Outline each Plasmodium falciparum-infected red blood cell.
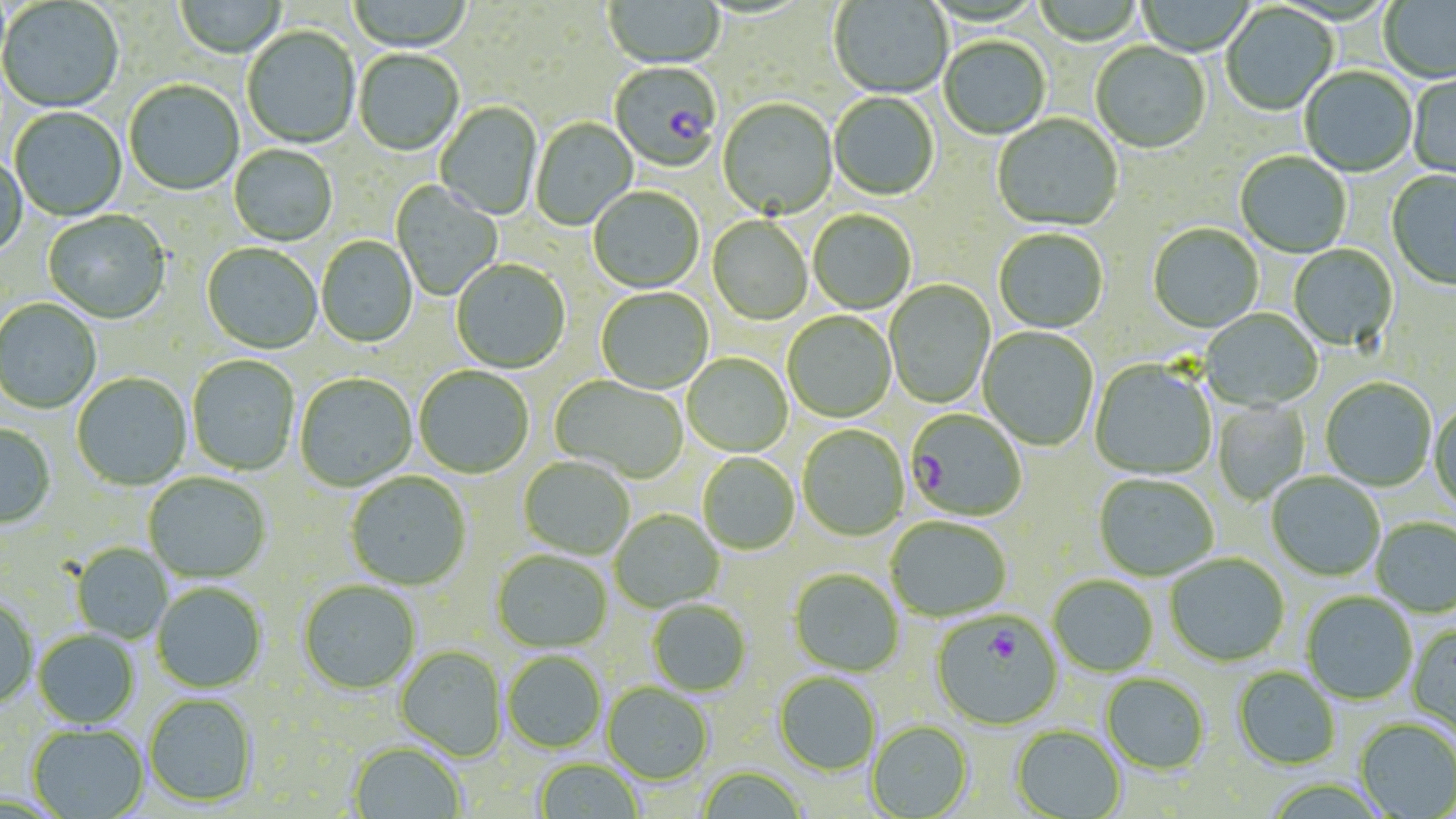

Approximate bounding boxes as named x1/y1/x2/y2 corners in pixels.
Plasmodium falciparum-infected red blood cells: (x1=609, y1=63, x2=721, y2=174), (x1=905, y1=410, x2=1026, y2=522), (x1=932, y1=612, x2=1061, y2=730).

Summary:
  - Uninfected red blood cell locations: (x1=174, y1=0, x2=286, y2=59), (x1=347, y1=0, x2=473, y2=53), (x1=1030, y1=0, x2=1145, y2=47), (x1=1135, y1=0, x2=1257, y2=56), (x1=1379, y1=0, x2=1456, y2=85), (x1=0, y1=1, x2=124, y2=115), (x1=604, y1=1, x2=726, y2=71), (x1=829, y1=1, x2=952, y2=100), (x1=1220, y1=4, x2=1338, y2=117), (x1=242, y1=27, x2=360, y2=150), (x1=939, y1=38, x2=1051, y2=141), (x1=1091, y1=42, x2=1211, y2=156), (x1=354, y1=50, x2=464, y2=157), (x1=1299, y1=68, x2=1417, y2=178), (x1=1408, y1=73, x2=1456, y2=182), (x1=124, y1=81, x2=244, y2=197), (x1=829, y1=93, x2=939, y2=201), (x1=717, y1=99, x2=838, y2=222), (x1=435, y1=102, x2=543, y2=221), (x1=10, y1=108, x2=127, y2=221), (x1=992, y1=115, x2=1123, y2=233), (x1=530, y1=117, x2=638, y2=231), (x1=228, y1=145, x2=337, y2=247), (x1=1235, y1=152, x2=1351, y2=258), (x1=0, y1=156, x2=27, y2=260), (x1=1387, y1=170, x2=1456, y2=292), (x1=391, y1=181, x2=502, y2=301), (x1=589, y1=188, x2=704, y2=294), (x1=42, y1=211, x2=171, y2=324), (x1=808, y1=211, x2=916, y2=315), (x1=707, y1=217, x2=813, y2=326), (x1=1148, y1=225, x2=1263, y2=334), (x1=994, y1=230, x2=1108, y2=335), (x1=316, y1=237, x2=418, y2=348), (x1=201, y1=244, x2=322, y2=355), (x1=1289, y1=245, x2=1398, y2=352), (x1=451, y1=260, x2=570, y2=373), (x1=885, y1=280, x2=995, y2=409), (x1=596, y1=289, x2=713, y2=395), (x1=0, y1=299, x2=101, y2=414), (x1=1201, y1=309, x2=1323, y2=411), (x1=783, y1=312, x2=896, y2=423), (x1=978, y1=327, x2=1098, y2=451), (x1=683, y1=354, x2=793, y2=457), (x1=187, y1=356, x2=299, y2=476), (x1=1090, y1=360, x2=1217, y2=481), (x1=414, y1=367, x2=534, y2=479), (x1=72, y1=373, x2=192, y2=491), (x1=295, y1=374, x2=417, y2=492), (x1=550, y1=376, x2=688, y2=483), (x1=1321, y1=378, x2=1436, y2=491), (x1=1212, y1=400, x2=1311, y2=505), (x1=1429, y1=402, x2=1456, y2=514), (x1=0, y1=424, x2=56, y2=529), (x1=798, y1=426, x2=909, y2=541), (x1=698, y1=454, x2=800, y2=555), (x1=519, y1=457, x2=634, y2=560), (x1=143, y1=472, x2=271, y2=583), (x1=345, y1=472, x2=471, y2=590), (x1=1266, y1=473, x2=1385, y2=581), (x1=1094, y1=475, x2=1219, y2=581), (x1=609, y1=511, x2=724, y2=613), (x1=886, y1=517, x2=1011, y2=622), (x1=1371, y1=518, x2=1456, y2=617), (x1=71, y1=543, x2=173, y2=643), (x1=492, y1=550, x2=612, y2=653), (x1=1165, y1=554, x2=1289, y2=667), (x1=789, y1=569, x2=904, y2=677), (x1=1049, y1=576, x2=1158, y2=676), (x1=298, y1=581, x2=420, y2=694), (x1=152, y1=583, x2=267, y2=693), (x1=1301, y1=592, x2=1417, y2=705), (x1=0, y1=598, x2=38, y2=709), (x1=647, y1=600, x2=751, y2=696), (x1=1407, y1=624, x2=1456, y2=738), (x1=34, y1=630, x2=139, y2=729), (x1=395, y1=645, x2=507, y2=761), (x1=503, y1=650, x2=606, y2=753), (x1=1233, y1=667, x2=1341, y2=769), (x1=773, y1=673, x2=880, y2=776), (x1=1101, y1=674, x2=1210, y2=775), (x1=602, y1=683, x2=714, y2=785), (x1=144, y1=694, x2=258, y2=807), (x1=1354, y1=719, x2=1456, y2=817), (x1=867, y1=721, x2=973, y2=818), (x1=27, y1=724, x2=149, y2=819), (x1=1011, y1=725, x2=1127, y2=818), (x1=348, y1=741, x2=465, y2=819), (x1=534, y1=759, x2=643, y2=818), (x1=696, y1=766, x2=809, y2=819)
  - Slide-level diagnosis: Plasmodium falciparum
  - Image size: 1456×819 pixels
  - Stain: May-Grünwald-Giemsa
  - Magnification: 1000x
  - Preparation: thin blood smear
  - Field of view: single
  - Modality: light microscopy